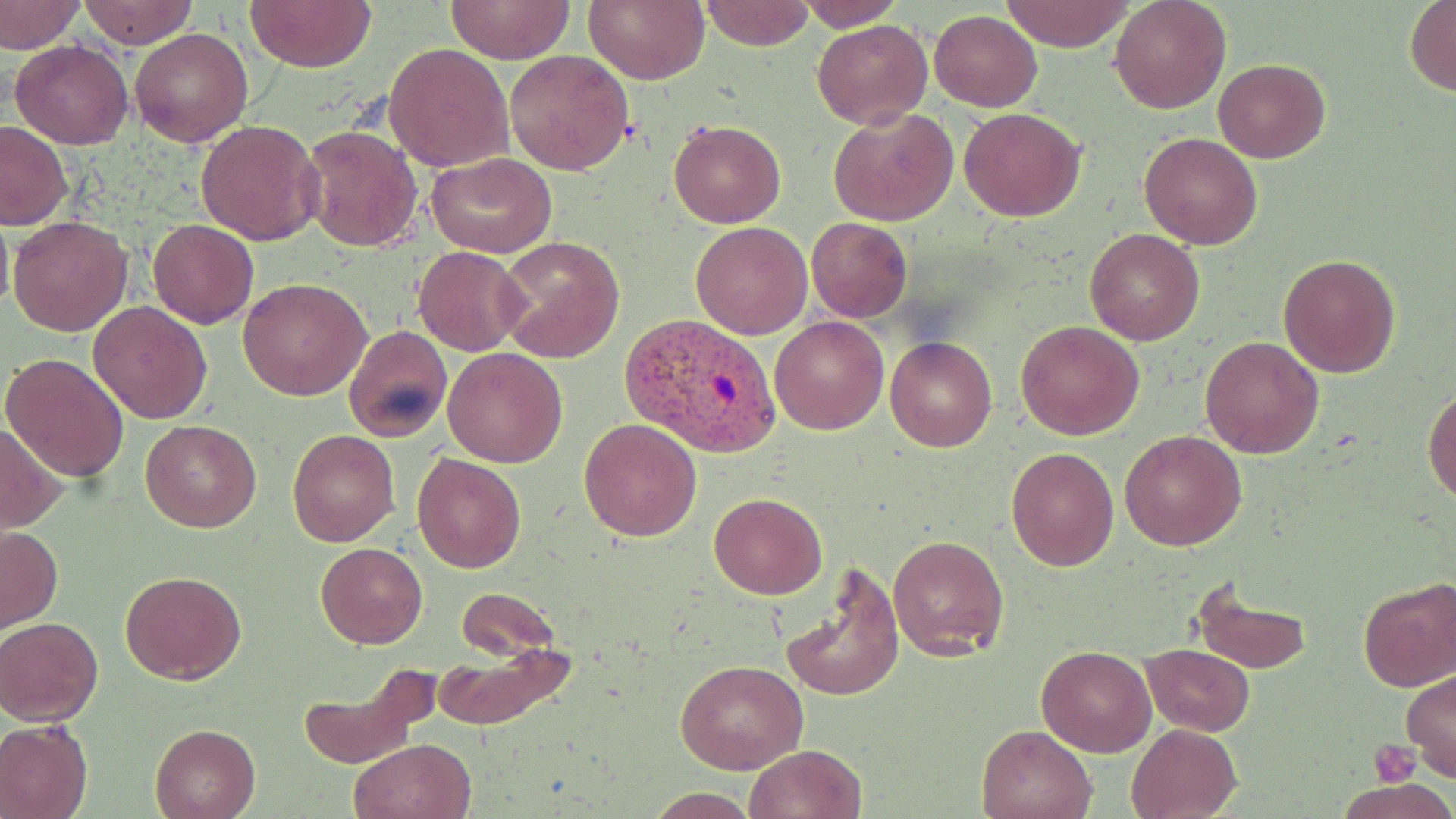 Approximate bounding boxes as [x1, y1, x2, y2] in pixels. Platelet locations: [1371, 741, 1419, 787]. Uninfected red blood cell locations: [78, 0, 196, 49], [245, 0, 376, 72], [447, 0, 574, 63], [586, 0, 709, 84], [700, 0, 816, 51], [795, 0, 903, 30], [1000, 0, 1135, 52], [1110, 0, 1230, 113], [2, 1, 83, 52], [1404, 2, 1455, 95], [930, 9, 1041, 110], [812, 20, 931, 128], [131, 28, 253, 147], [10, 41, 134, 149], [386, 43, 513, 172], [505, 49, 635, 175], [1212, 59, 1330, 163], [829, 105, 958, 226], [959, 107, 1086, 221], [195, 119, 326, 246], [669, 119, 785, 228], [0, 122, 73, 229], [299, 124, 423, 252], [1139, 132, 1263, 248], [427, 152, 556, 258], [0, 209, 13, 317], [7, 216, 131, 337], [806, 217, 912, 321], [148, 220, 258, 329], [690, 221, 812, 339], [1085, 228, 1203, 346], [495, 238, 625, 364], [412, 247, 529, 355], [1279, 253, 1400, 376], [239, 277, 371, 401], [88, 301, 213, 424], [770, 315, 890, 436], [1016, 320, 1145, 439], [342, 326, 452, 443], [1200, 336, 1325, 458], [885, 337, 997, 452], [442, 347, 567, 466], [1, 353, 130, 481], [1424, 386, 1456, 504], [578, 419, 702, 541], [140, 420, 261, 532], [0, 421, 70, 530], [287, 429, 398, 545], [1123, 430, 1245, 549], [1006, 439, 1238, 556], [1006, 447, 1119, 571], [411, 452, 526, 574], [709, 494, 827, 599], [0, 525, 62, 632], [887, 533, 1010, 662], [316, 542, 428, 648], [777, 564, 902, 703], [120, 570, 247, 683], [1188, 579, 1314, 674], [1358, 579, 1456, 692], [454, 588, 561, 662], [0, 616, 104, 725], [429, 638, 576, 731], [1140, 643, 1254, 736], [1037, 645, 1157, 756], [675, 658, 806, 773], [1402, 670, 1456, 783], [294, 677, 425, 769], [0, 718, 92, 819], [150, 723, 259, 818], [1126, 723, 1242, 819], [975, 724, 1097, 819], [349, 738, 475, 819], [743, 744, 868, 819], [1340, 781, 1453, 818]. Plasmodium vivax-infected red blood cell locations: [618, 312, 780, 458]. Slide-level diagnosis: Plasmodium vivax. May-Grünwald-Giemsa-stained preparation. Thin blood film. Image is 1456×819 pixels. 1000x magnification. Single field of view. Light microscopy.